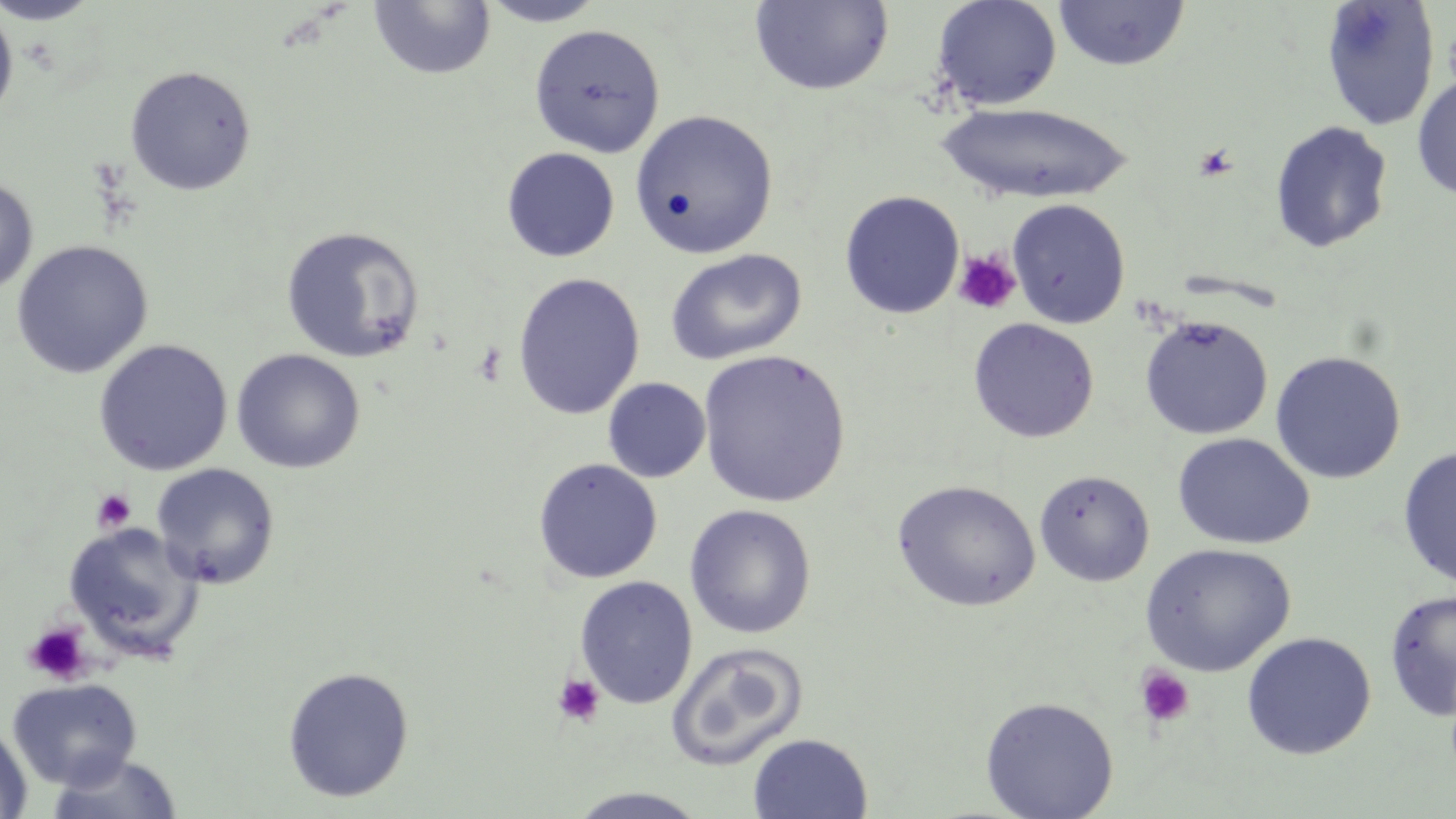

{
  "slide_level_diagnosis": "negative for blood parasites",
  "uninfected_red_blood_cell_locations": "approximate bounding boxes as named x1/y1/x2/y2 corners in pixels: (x1=0, y1=0, x2=105, y2=25), (x1=476, y1=0, x2=611, y2=27), (x1=932, y1=0, x2=1062, y2=111), (x1=1053, y1=0, x2=1190, y2=71), (x1=1320, y1=0, x2=1440, y2=131), (x1=368, y1=1, x2=496, y2=80), (x1=749, y1=1, x2=894, y2=95), (x1=0, y1=4, x2=18, y2=126), (x1=528, y1=24, x2=665, y2=158), (x1=124, y1=65, x2=256, y2=195), (x1=1412, y1=75, x2=1456, y2=200), (x1=937, y1=102, x2=1131, y2=204), (x1=629, y1=110, x2=779, y2=259), (x1=1269, y1=120, x2=1393, y2=254), (x1=501, y1=147, x2=620, y2=262), (x1=0, y1=175, x2=38, y2=297), (x1=839, y1=190, x2=965, y2=319), (x1=1007, y1=199, x2=1130, y2=329), (x1=281, y1=225, x2=426, y2=364), (x1=11, y1=240, x2=154, y2=378), (x1=664, y1=249, x2=808, y2=365), (x1=512, y1=272, x2=646, y2=420), (x1=1139, y1=314, x2=1273, y2=439), (x1=967, y1=318, x2=1099, y2=443), (x1=93, y1=339, x2=233, y2=475), (x1=231, y1=349, x2=365, y2=474), (x1=697, y1=349, x2=851, y2=509), (x1=1270, y1=350, x2=1406, y2=484), (x1=603, y1=377, x2=711, y2=483), (x1=1172, y1=432, x2=1315, y2=550), (x1=1397, y1=446, x2=1456, y2=590), (x1=533, y1=458, x2=663, y2=584), (x1=151, y1=463, x2=280, y2=589), (x1=1034, y1=469, x2=1155, y2=586), (x1=891, y1=480, x2=1041, y2=612), (x1=684, y1=504, x2=816, y2=638), (x1=63, y1=522, x2=204, y2=661), (x1=1139, y1=543, x2=1296, y2=677), (x1=574, y1=576, x2=698, y2=709), (x1=1383, y1=589, x2=1456, y2=723), (x1=1241, y1=632, x2=1377, y2=760), (x1=666, y1=642, x2=809, y2=771), (x1=282, y1=666, x2=415, y2=802), (x1=6, y1=677, x2=143, y2=790), (x1=980, y1=696, x2=1119, y2=818), (x1=0, y1=720, x2=34, y2=819), (x1=747, y1=733, x2=873, y2=818), (x1=45, y1=753, x2=184, y2=818), (x1=563, y1=787, x2=713, y2=819)",
  "magnification": "1000x",
  "platelet_locations": "approximate bounding boxes as named x1/y1/x2/y2 corners in pixels: (x1=1443, y1=20, x2=1456, y2=98), (x1=1193, y1=145, x2=1238, y2=181), (x1=953, y1=249, x2=1021, y2=315), (x1=91, y1=488, x2=136, y2=533), (x1=22, y1=622, x2=92, y2=686), (x1=1134, y1=666, x2=1196, y2=728), (x1=553, y1=673, x2=605, y2=727)",
  "field_of_view": "one of a larger specimen",
  "stain": "May-Grünwald-Giemsa",
  "image_size": "1456×819 pixels",
  "preparation": "thin blood smear",
  "modality": "light microscopy"
}